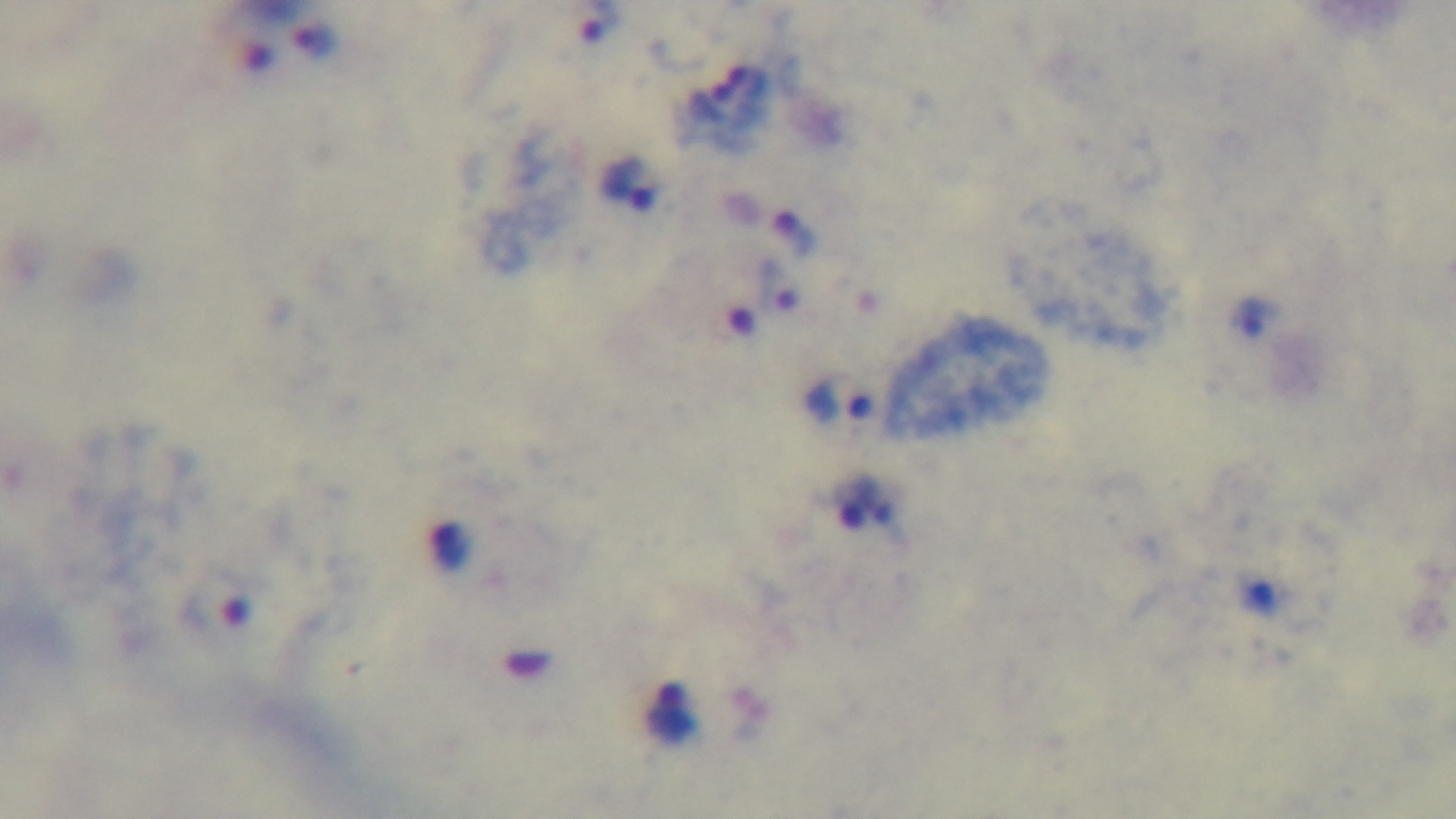
Summary:
  - Objective: 100x oil immersion
  - Capture: mounted 4K digital camera
  - Preparation: thick smear
  - Stain: Giemsa
  - Malaria status: infected
  - Field of view: one from the slide
  - Modality: light microscopy